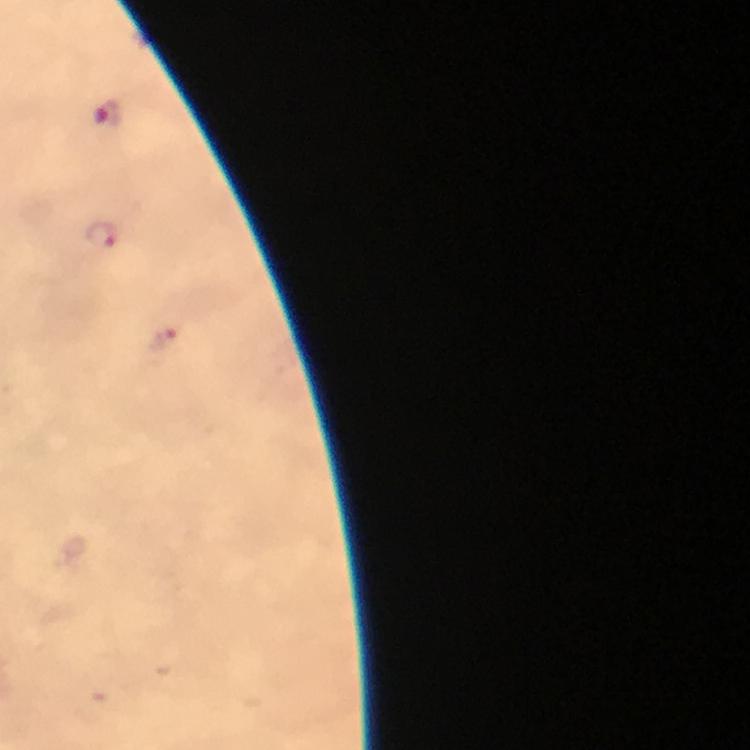
Approximate object centers, in pixels from the top-left corner. Malaria parasite locations: (x=106, y=114), (x=103, y=237), (x=163, y=339). Image is 750×750 pixels. Immersion oil applied. From a malaria diagnostic workup. A crop from one field of view. At 100x magnification. Photographed through the microscope with a smartphone camera. Thick blood smear. Giemsa-stained preparation.